Point out each Plasmodium parasite.
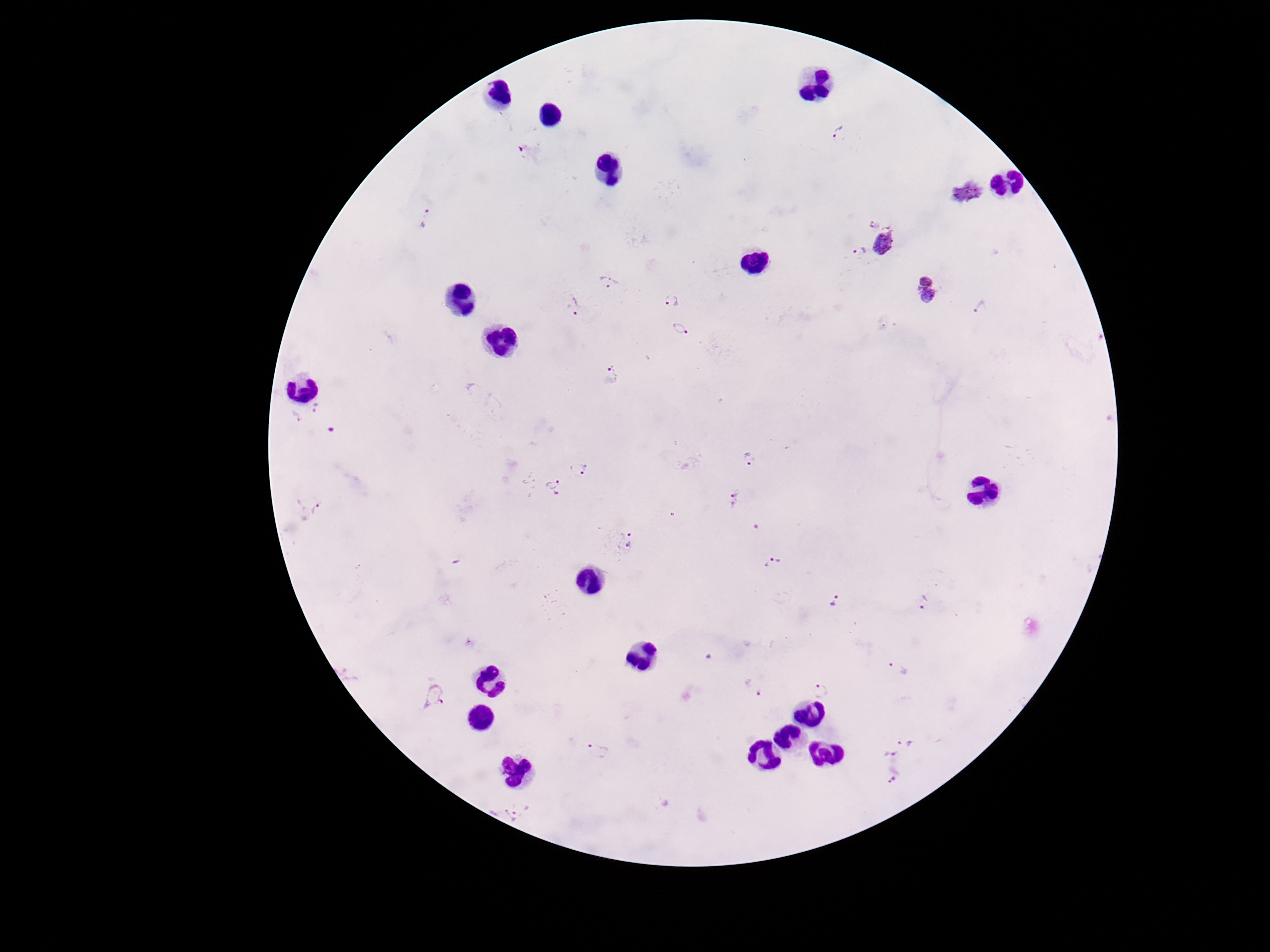
Approximate object centers, in pixels from the top-left corner.
Plasmodium parasites: (x=841, y=136), (x=967, y=192), (x=426, y=218), (x=873, y=223), (x=885, y=243), (x=860, y=252), (x=607, y=282), (x=926, y=290), (x=672, y=302), (x=575, y=306), (x=981, y=307), (x=680, y=329), (x=613, y=374), (x=316, y=408), (x=296, y=417), (x=332, y=431), (x=749, y=459), (x=579, y=469), (x=552, y=488), (x=737, y=498), (x=311, y=507), (x=619, y=542), (x=772, y=563), (x=835, y=602), (x=925, y=602), (x=897, y=667), (x=755, y=688), (x=821, y=690), (x=436, y=694), (x=907, y=740), (x=598, y=751), (x=890, y=755), (x=893, y=778), (x=516, y=810).

Smartphone photograph taken through the microscope eyepiece. Thick peripheral-blood smear. Patient malaria status: infected. One field from this slide. Image is 1270×952 pixels. 100x magnification. Giemsa-stained preparation.